Comment on the morphology of the red blood cells.
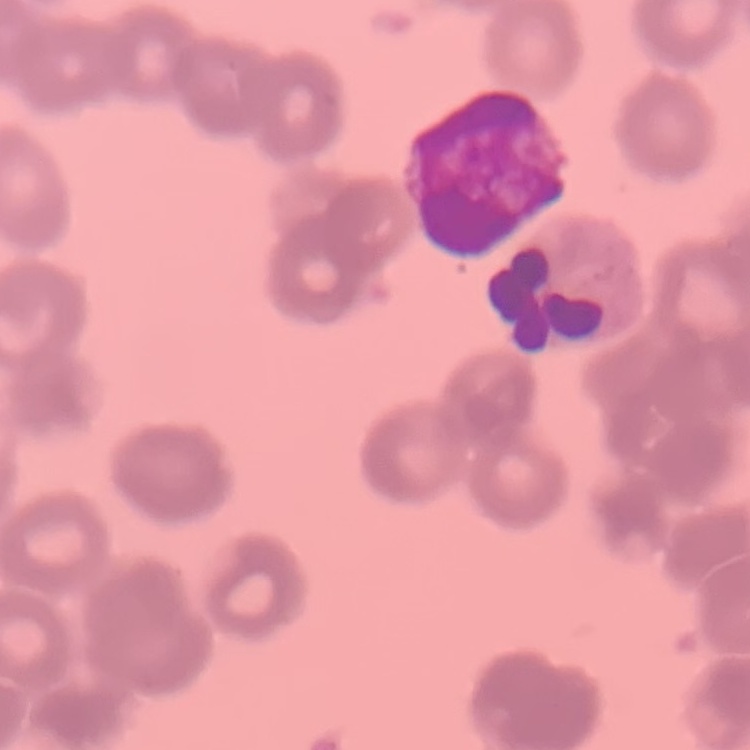
Rouleaux formation.

Summary:
  - Stain: Field's or Giemsa
  - Image type: square crop of a larger photomicrograph
  - Preparation: thin blood smear